Identify the preparation type.
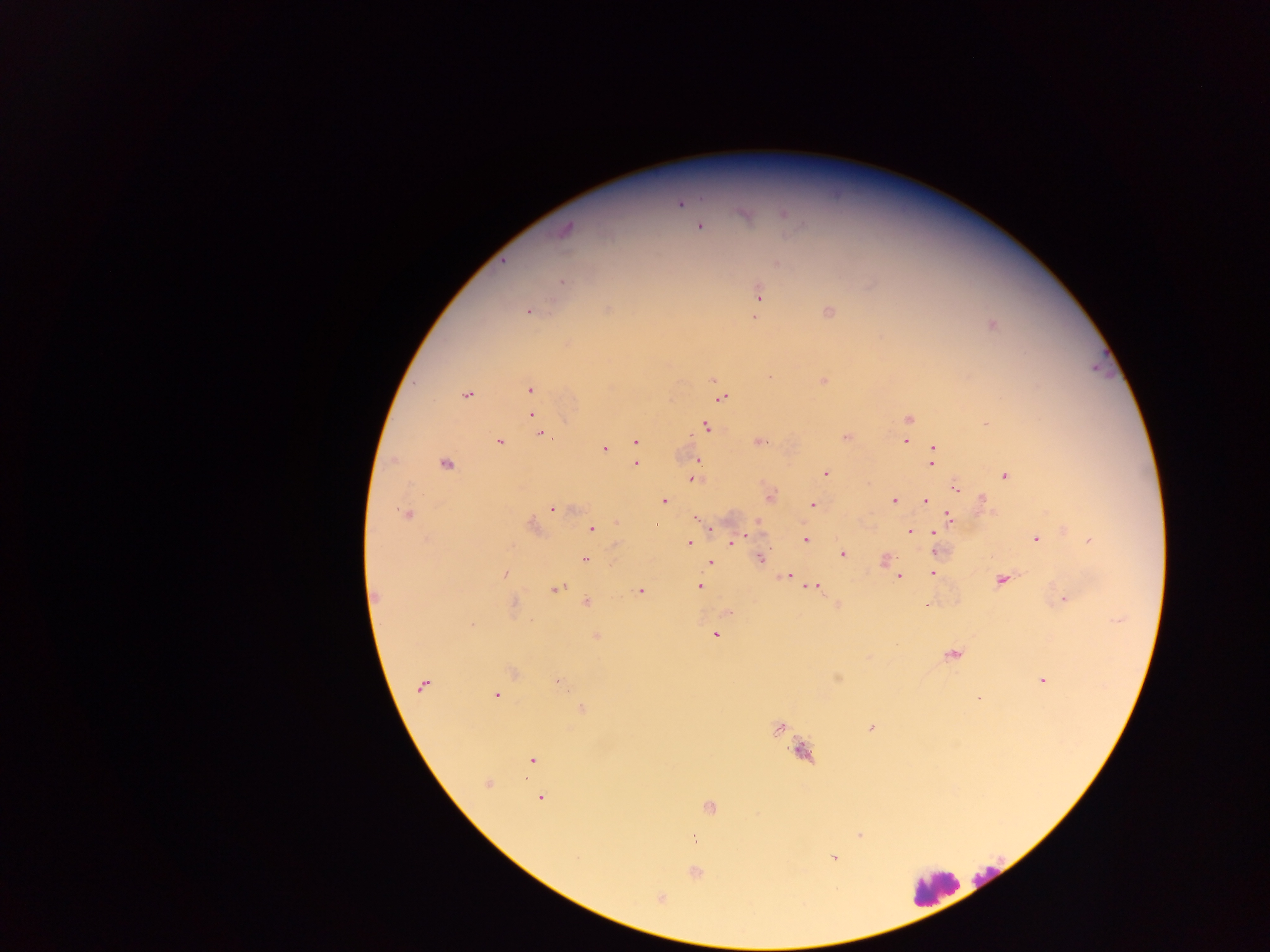

Thick blood smear.

capture = mobile-phone photograph through a microscope
Plasmodium parasite locations = approximate centers as {x, y} in pixels: {680, 204}, {785, 214}, {700, 226}, {566, 230}, {562, 283}, {758, 294}, {757, 305}, {607, 309}, {527, 311}, {828, 312}, {755, 317}, {992, 325}, {713, 380}, {823, 381}, {530, 389}, {466, 395}, {722, 398}, {532, 416}, {908, 419}, {707, 427}, {541, 434}, {845, 437}, {636, 441}, {759, 442}, {906, 442}, {499, 443}, {605, 449}, {933, 449}, {697, 460}, {445, 463}, {637, 464}, {931, 464}, {826, 473}, {1004, 476}, {694, 478}, {956, 489}, {770, 496}, {926, 500}, {983, 500}, {664, 501}, {894, 501}, {813, 505}, {551, 509}, {405, 514}, {696, 517}, {949, 518}, {758, 523}, {657, 525}, {533, 527}, {712, 528}, {591, 529}, {910, 531}, {934, 532}, {806, 539}, {1036, 539}, {1091, 541}, {689, 543}, {733, 543}, {935, 551}, {843, 554}, {760, 558}, {585, 559}, {885, 560}, {711, 562}, {933, 573}, {505, 574}, {787, 576}, {898, 576}, {1001, 580}, {700, 586}, {814, 586}, {555, 588}, {640, 591}, {374, 595}, {1065, 599}, {588, 602}, {838, 604}, {926, 606}, {472, 625}, {597, 635}, {715, 635}, {953, 655}, {514, 672}, {838, 678}, {1043, 681}, {423, 685}, {560, 685}, {496, 696}, {978, 698}, {583, 708}, {779, 727}, {870, 728}, {802, 753}, {532, 760}, {487, 783}, {542, 798}, {710, 807}, {860, 834}, {834, 858}, {695, 873}, {660, 898}
country = Ghana
leukocyte locations = approximate centers as {x, y} in pixels: {932, 887}
field of view = single
image size = 1270×952 pixels